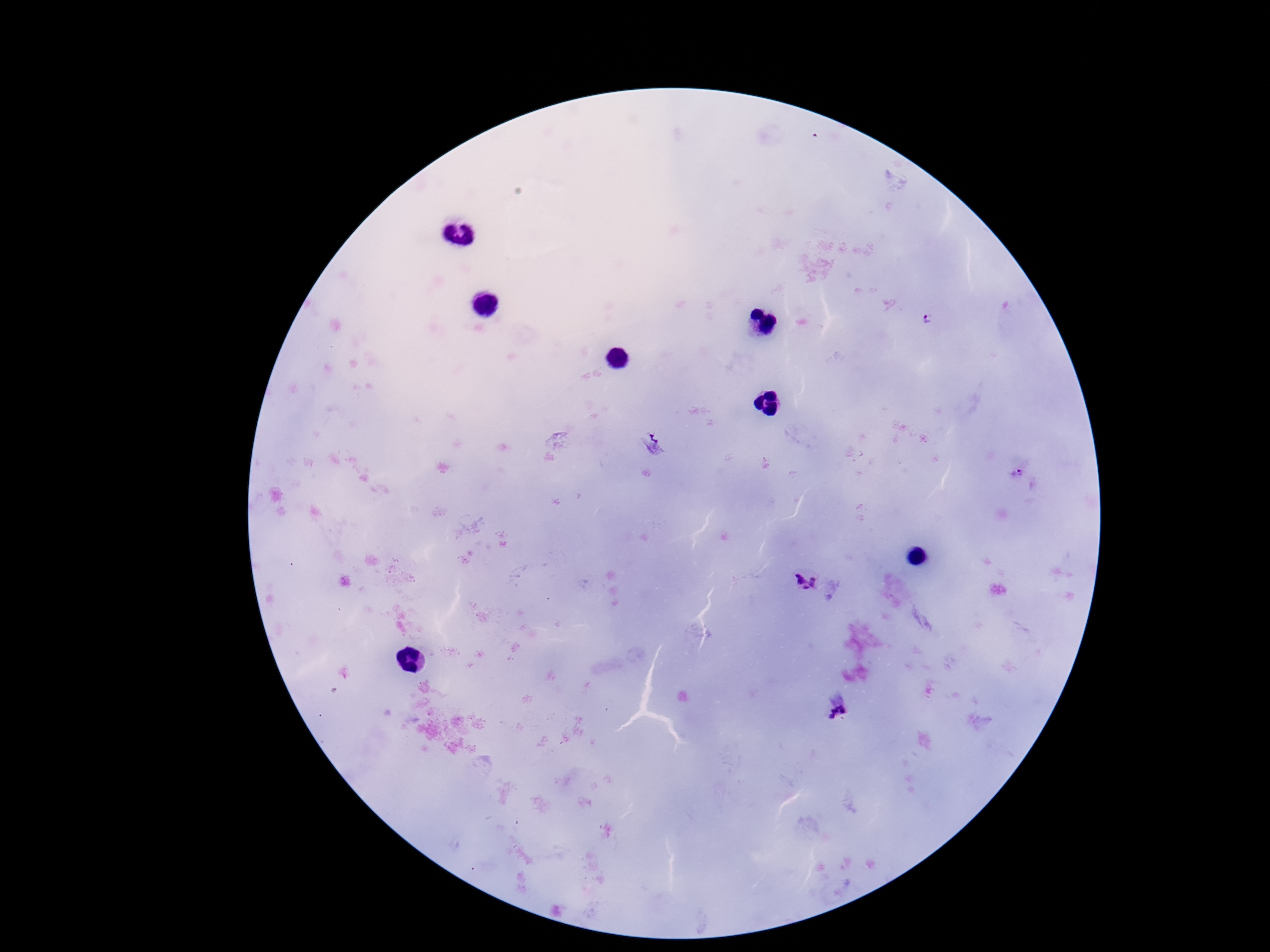

capture = smartphone camera through the microscope eyepiece
stain = Giemsa
image size = 1270×952 pixels
Plasmodium parasite locations = approximate centers as {x, y} in pixels: {926, 317}, {651, 445}, {1016, 473}, {808, 577}, {838, 713}
magnification = 100x
preparation = thick blood film
patient malaria status = infected
field of view = single